Name the cell type shown.
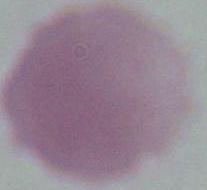

This is an erythrocyte.

modality = photomicrograph
magnification = 1000x